Assess this cell for malaria.
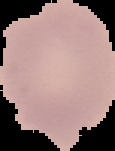
Uninfected.

Segmented cell region on a black background. Image is 115×151 pixels. From a thin blood film.